Comment on the morphology of the red blood cells.
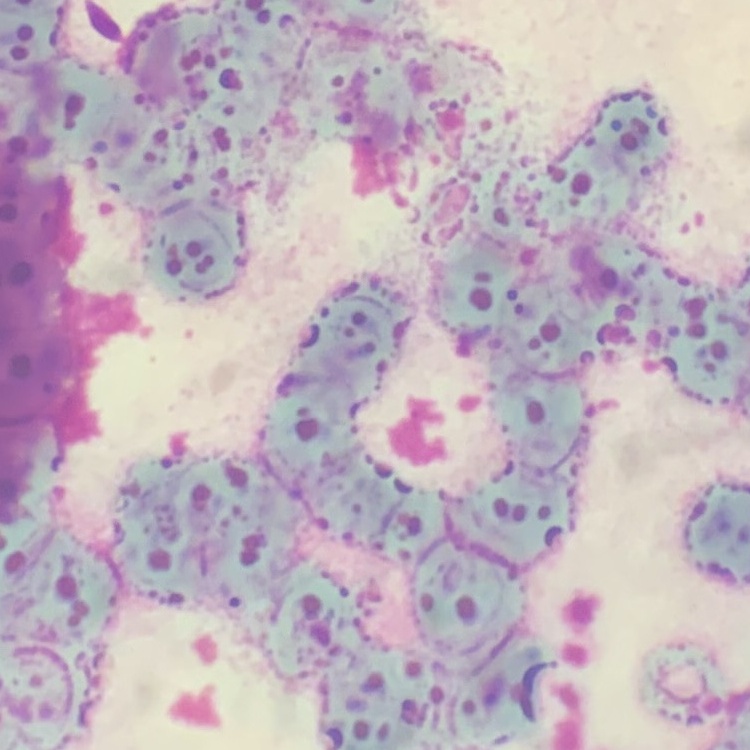
They show rouleaux formation.

Summary:
  - Image type: one tile cut from a larger photomicrograph
  - Stain: Field's or Giemsa
  - Preparation: thin peripheral smear